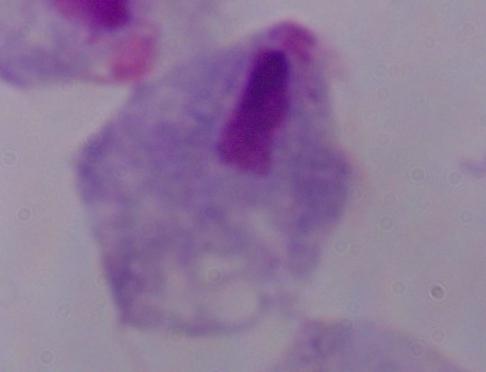
identification = trichomonad
magnification = 1000x
modality = micrograph